Report the malaria status of this cell.
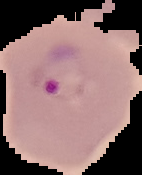
It is parasitized.

Segmented cell region on a black background. From a thin blood film. Image is 142×175 pixels.